Report the malaria status.
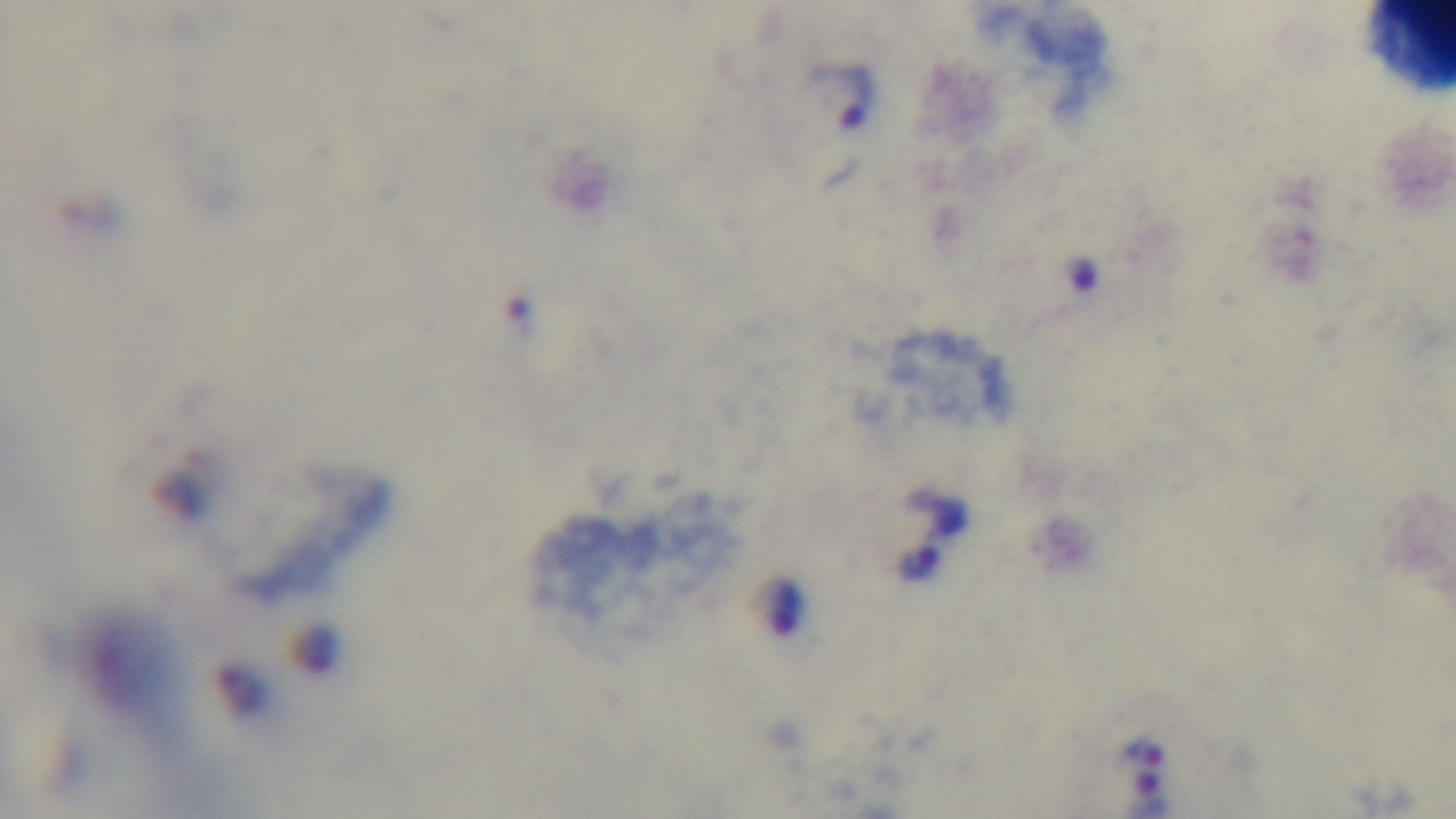

It is infected.

Giemsa-stained. Oil-immersion objective, 100x. Light microscopy. Single field of view. Captured with a mounted 4K digital camera. Preparation: thick blood film.